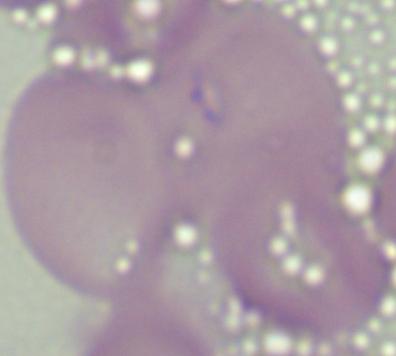
Summary:
  - Identification: Babesia
  - Magnification: 1000x
  - Modality: micrograph